Report the malaria status of this cell.
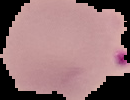
It is parasitized.

image_type: segmented cell region on a black background
image_size: 130×100 pixels
preparation: thin blood film